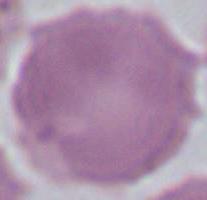
Summary:
  - Identification: red blood cell
  - Magnification: 1000x
  - Modality: photomicrograph